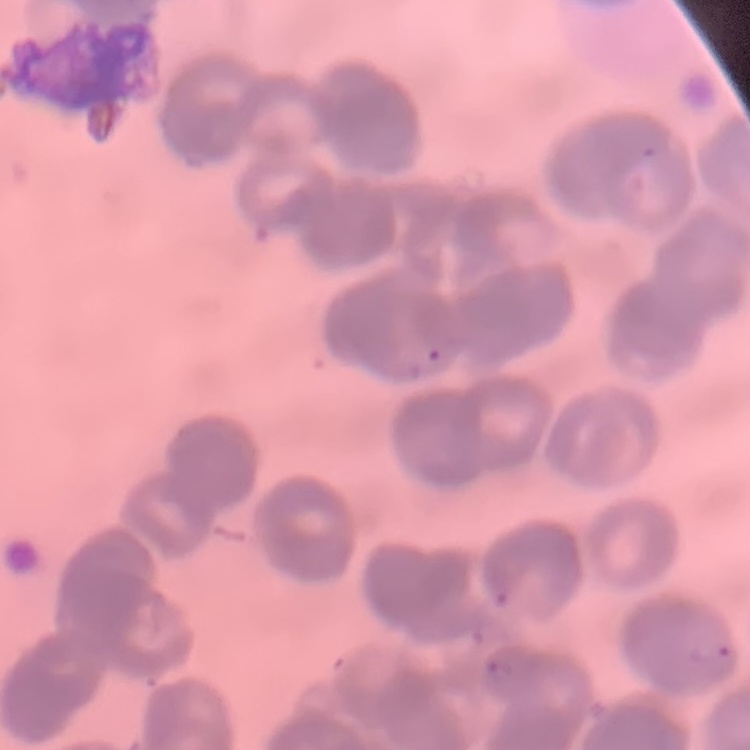

red blood cell morphology = rouleaux formation
preparation = thin blood smear
image type = square crop of a larger photomicrograph
stain = Field's or Giemsa